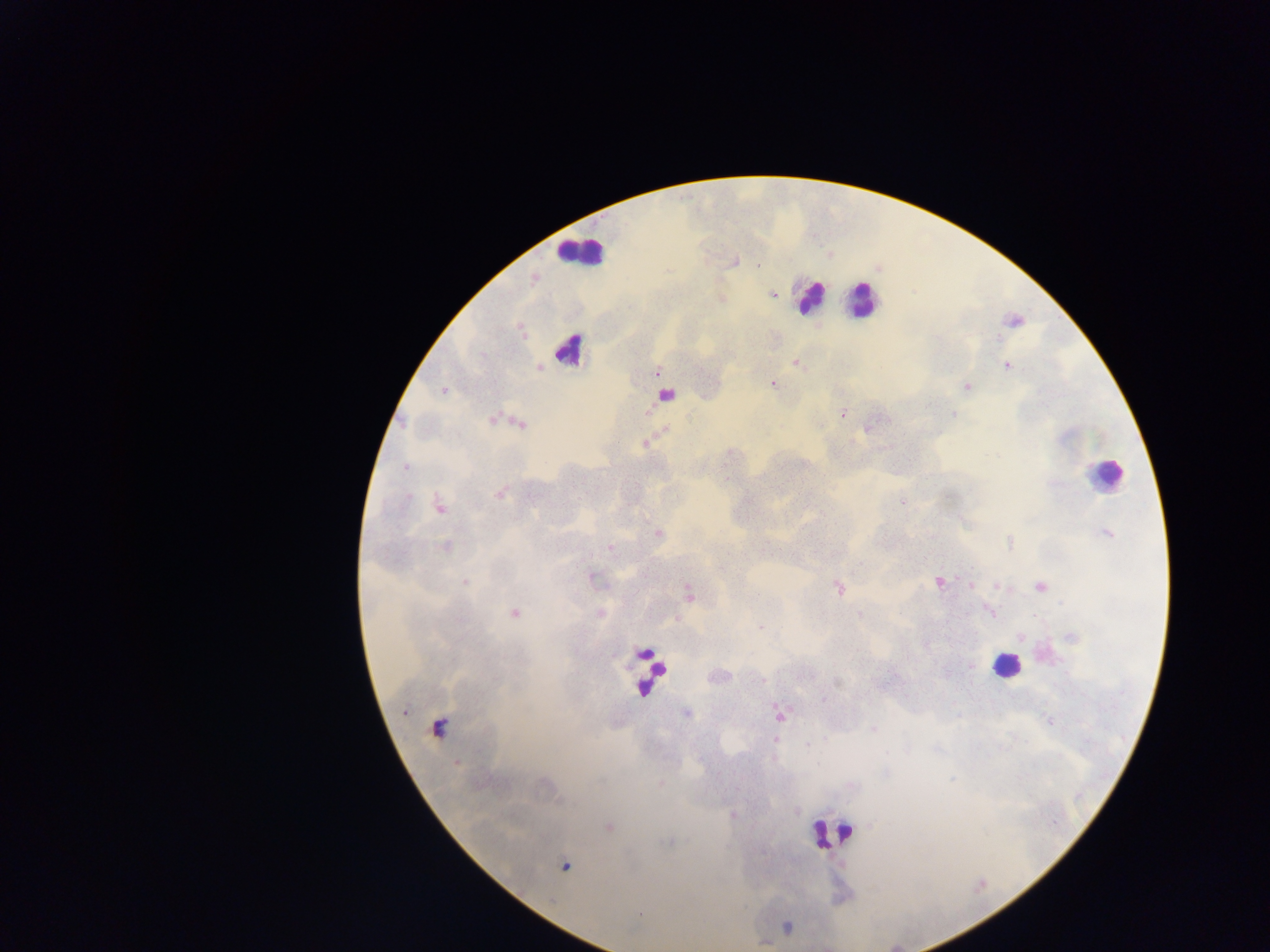

image size = 1270×952 pixels
leukocyte locations = approximate centers as x y in pixels: 578 251; 809 296; 862 300; 569 350; 1104 474; 1006 665; 646 672; 831 834
Plasmodium parasite locations = approximate centers as x y in pixels: 734 262; 757 266; 772 295; 998 338; 795 362; 1007 366; 539 368; 657 372; 772 384; 967 387; 444 390; 842 414; 953 414; 646 444; 406 467; 500 493; 408 497; 903 503; 440 507; 658 533; 1107 533; 1010 543; 445 547; 610 547; 592 576; 465 581; 939 582; 971 585; 998 587; 1040 587; 839 588; 688 592; 514 612; 991 613; 860 614; 761 627; 1020 638; 1071 638; 970 665; 838 682; 822 699; 687 713; 779 715; 1050 721; 439 726; 873 729; 774 740; 806 744; 456 762; 608 827; 565 866
capture = mobile-phone photograph through a microscope
country = Ghana
field of view = single
preparation = thick blood smear